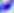

Summary:
  - Magnification: 400x
  - Identification: Toxoplasma gondii
  - Modality: photomicrograph